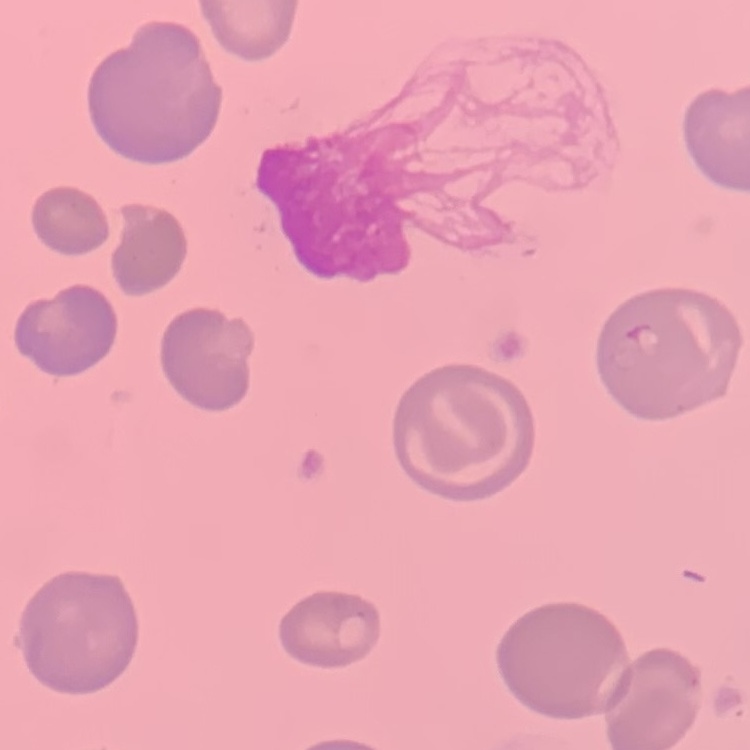
erythrocyte_morphology: no rouleaux formation
image_type: square crop of a larger photomicrograph
preparation: thin blood smear
stain: Field's or Giemsa